Give the position of every leukocyte visible.
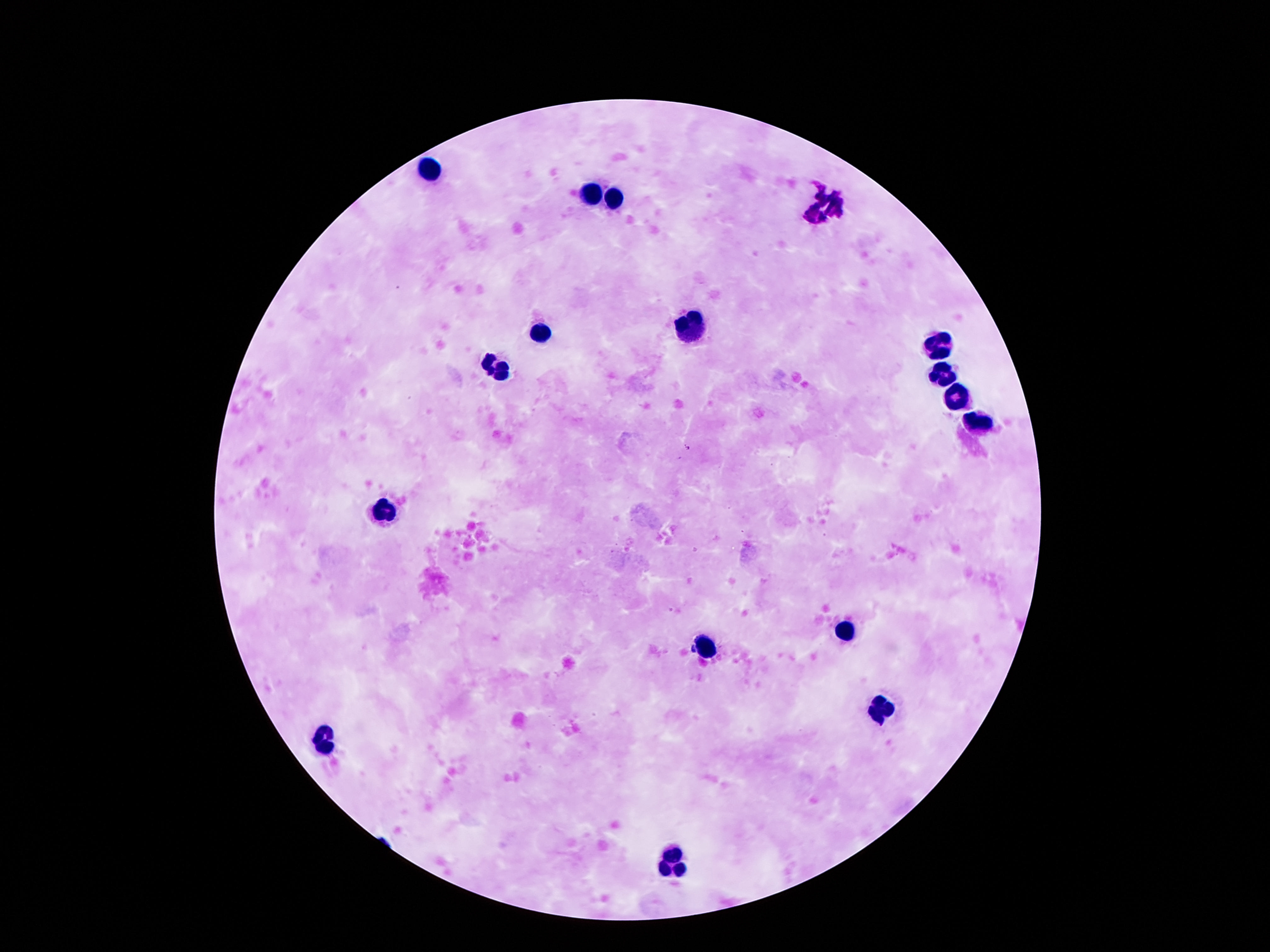
Approximate centers as (x, y) in pixels.
Leukocytes: (431, 170), (592, 195), (614, 199), (692, 329), (542, 331), (939, 344), (497, 369), (940, 377), (955, 397), (977, 425), (387, 513), (844, 627), (707, 651), (880, 709), (323, 742), (676, 864).

{
  "capture": "smartphone camera through the microscope eyepiece",
  "stain": "Giemsa",
  "patient_malaria_status": "uninfected",
  "preparation": "thick peripheral-blood smear",
  "magnification": "100x",
  "field_of_view": "one from this slide",
  "image_size": "1270×952 pixels"
}